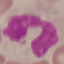 Malaria status: uninfected. Thin blood film. Cell patch, automatically extracted from a larger field of view and resized to 64 × 64 pixels. Giemsa stain. Photographed with a smartphone camera at the microscope eyepiece.